State which parasite is depicted.
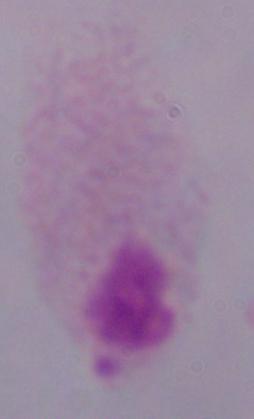

This is a trichomonad.

Photomicrograph. Captured at 1000x magnification.